Identify the parasite.
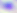
This is Toxoplasma gondii.

Micrograph. Captured at 400x magnification.